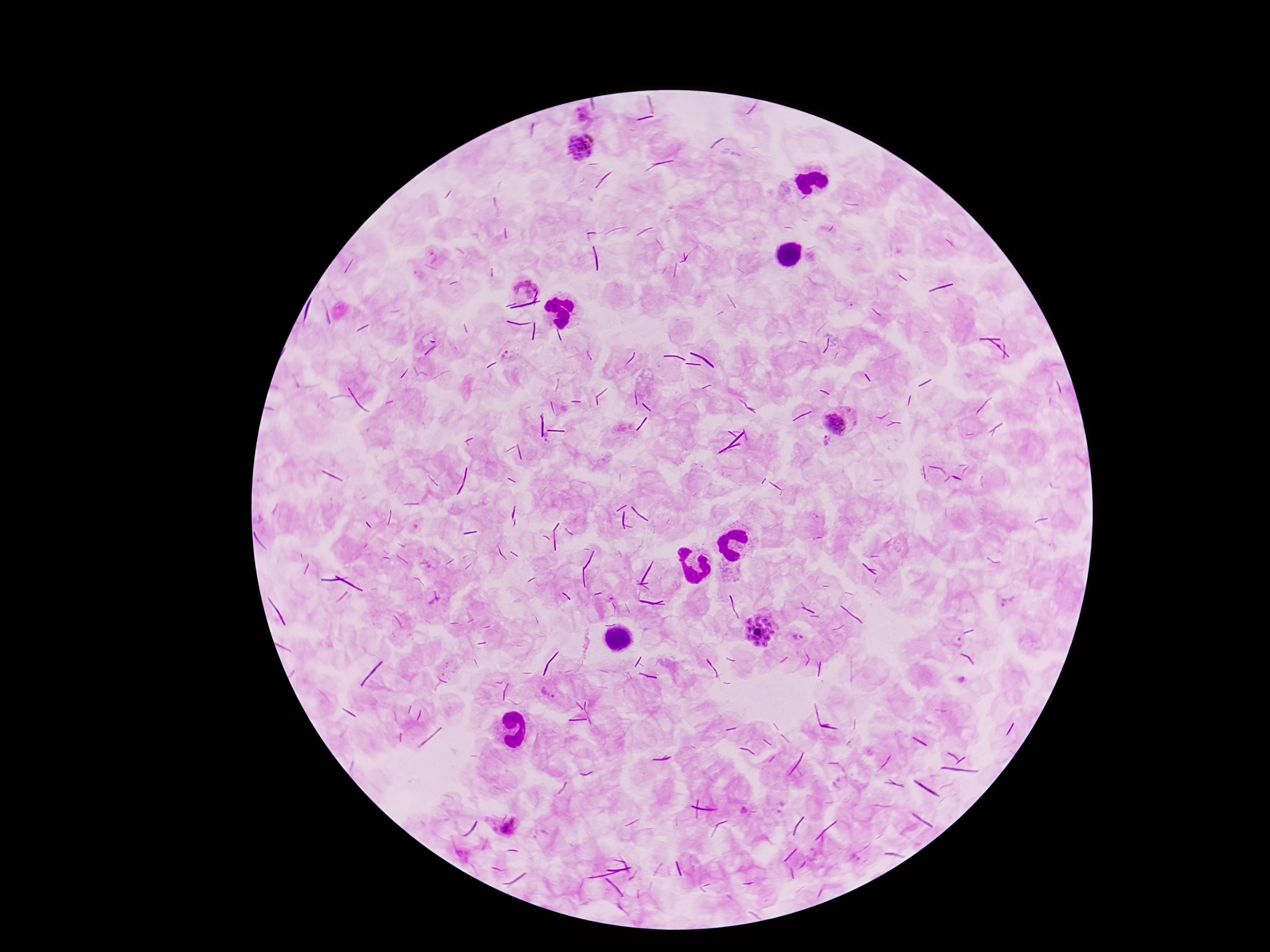 Approximate object centers, in pixels from the top-left corner. Plasmodium parasite locations: (x=583, y=118), (x=581, y=146), (x=526, y=286), (x=836, y=422), (x=827, y=441), (x=1008, y=599), (x=760, y=632), (x=798, y=638), (x=959, y=642), (x=502, y=819). Single field of view. Patient malaria status: infected. Giemsa-stained preparation. Image is 1270×952 pixels. Thick blood film. 100x magnification. Photographed through the microscope eyepiece with a smartphone camera.